Report the malaria status of this cell.
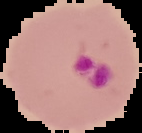
It is parasitized.

The area outside the segmented cell region is set to black. From a thin blood smear. Image is 142×133 pixels.